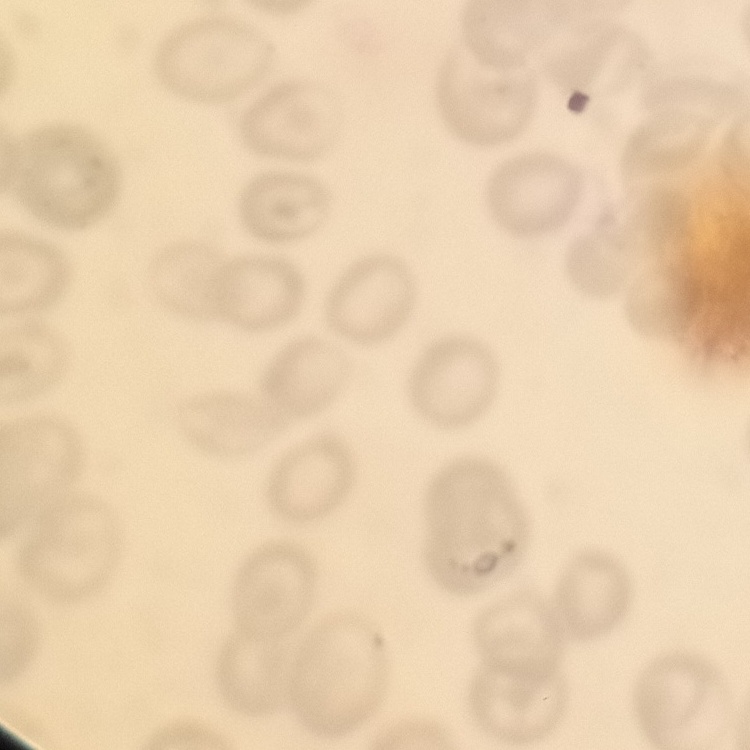

red blood cell morphology = no rouleaux formation
image type = square crop of a larger photomicrograph
preparation = thin blood film
stain = Field's or Giemsa